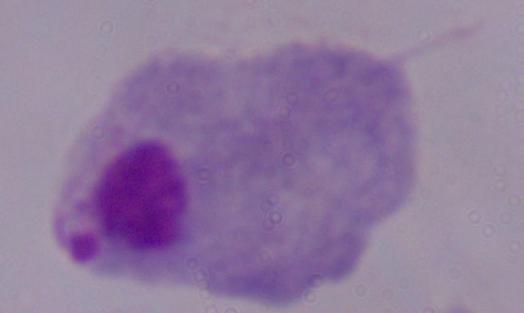

Summary:
  - Modality: micrograph
  - Identification: trichomonad
  - Magnification: 1000x